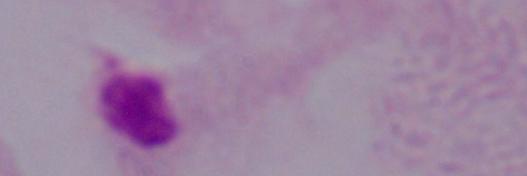

{
  "identification": "trichomonad",
  "magnification": "1000x",
  "modality": "photomicrograph"
}